Classify this cell by malaria status.
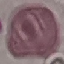
Uninfected.

image type = cell patch, automatically extracted from a larger field of view and resized to 64 × 64 pixels
stain = Giemsa
capture = smartphone camera at the microscope eyepiece
preparation = thin blood smear